Outline each uninfected red blood cell.
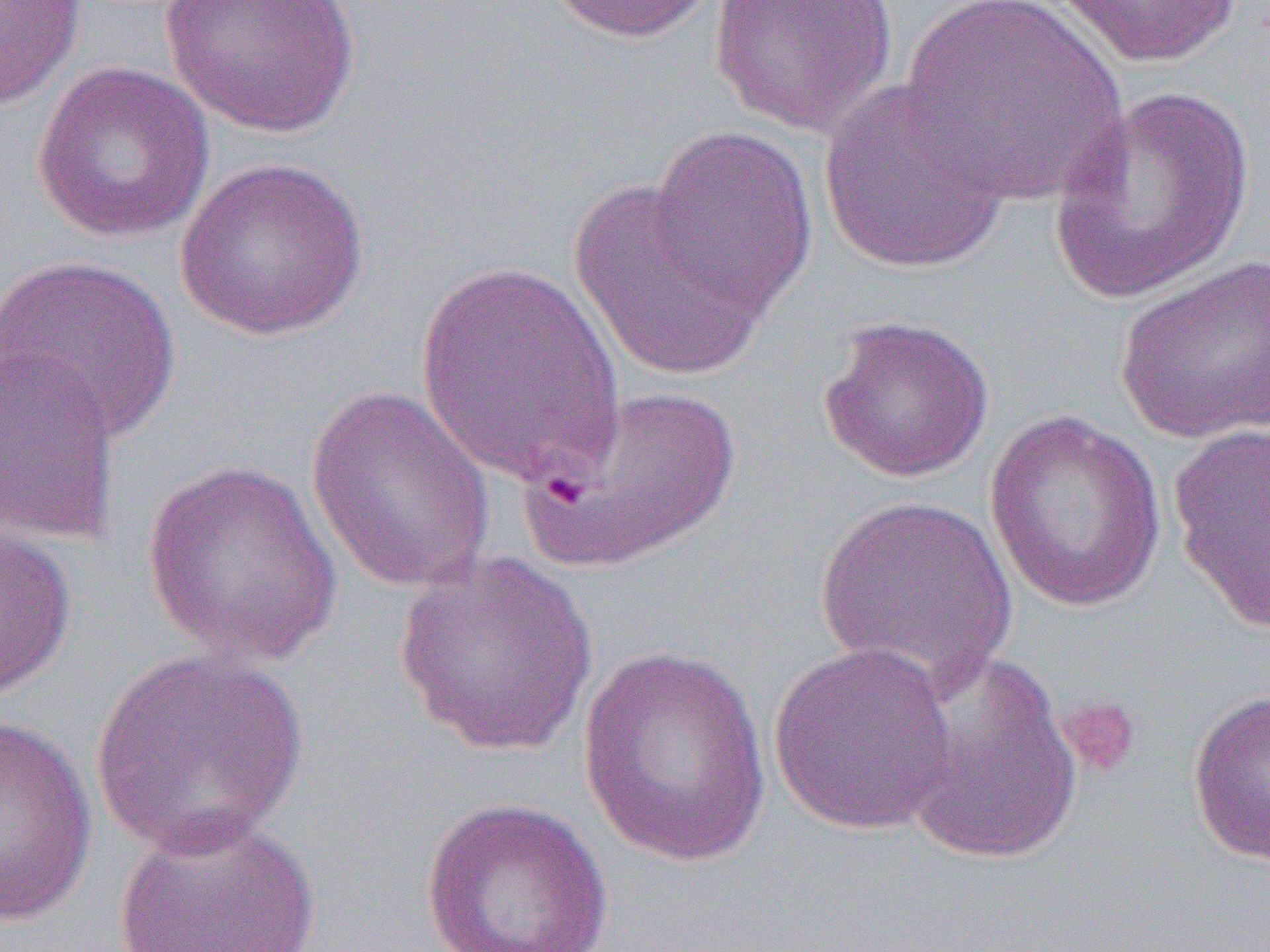
Approximate bounding boxes as named x1/y1/x2/y2 corners in pixels.
Uninfected red blood cells: (x1=0, y1=0, x2=87, y2=110), (x1=161, y1=0, x2=360, y2=137), (x1=540, y1=0, x2=723, y2=44), (x1=708, y1=0, x2=899, y2=137), (x1=1049, y1=0, x2=1245, y2=69), (x1=900, y1=1, x2=1126, y2=206), (x1=31, y1=60, x2=215, y2=243), (x1=818, y1=78, x2=1013, y2=274), (x1=1047, y1=85, x2=1257, y2=306), (x1=649, y1=124, x2=818, y2=317), (x1=175, y1=156, x2=370, y2=341), (x1=567, y1=181, x2=771, y2=382), (x1=0, y1=253, x2=182, y2=445), (x1=1112, y1=253, x2=1270, y2=446), (x1=413, y1=260, x2=628, y2=491), (x1=817, y1=313, x2=996, y2=484), (x1=0, y1=344, x2=123, y2=546), (x1=526, y1=384, x2=743, y2=572), (x1=304, y1=385, x2=497, y2=595), (x1=983, y1=411, x2=1168, y2=613), (x1=1168, y1=420, x2=1270, y2=633), (x1=141, y1=460, x2=344, y2=669), (x1=811, y1=494, x2=1018, y2=697), (x1=0, y1=517, x2=77, y2=701), (x1=393, y1=549, x2=599, y2=757), (x1=577, y1=641, x2=774, y2=865), (x1=767, y1=642, x2=959, y2=836), (x1=88, y1=650, x2=310, y2=860), (x1=894, y1=650, x2=1084, y2=866), (x1=1187, y1=688, x2=1269, y2=867), (x1=0, y1=716, x2=97, y2=928), (x1=419, y1=795, x2=616, y2=952), (x1=112, y1=812, x2=322, y2=952).

Summary:
  - Platelet locations: (x1=1056, y1=695, x2=1140, y2=780)
  - Slide-level diagnosis: Plasmodium falciparum
  - Preparation: thin blood film
  - Field of view: single
  - Modality: light microscopy
  - Magnification: 1000x
  - Image size: 1270×952 pixels